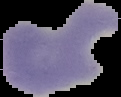
Image is 121×97 pixels. Result: malaria parasites detected. The area outside the segmented cell region is set to black. From a thin blood smear.